Assess this cell for malaria.
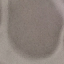
Uninfected.

Summary:
  - Image type: cell patch, automatically extracted from a larger field of view and resized to 64 × 64 pixels
  - Stain: Giemsa
  - Preparation: thin smear
  - Capture: smartphone camera at the microscope eyepiece